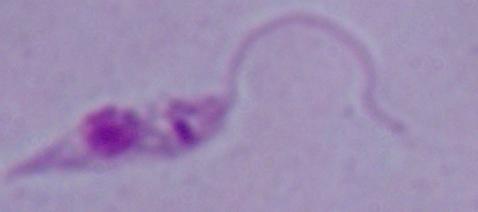
Summary:
  - Modality: micrograph
  - Magnification: 1000x
  - Identification: Leishmania